Locate platelets.
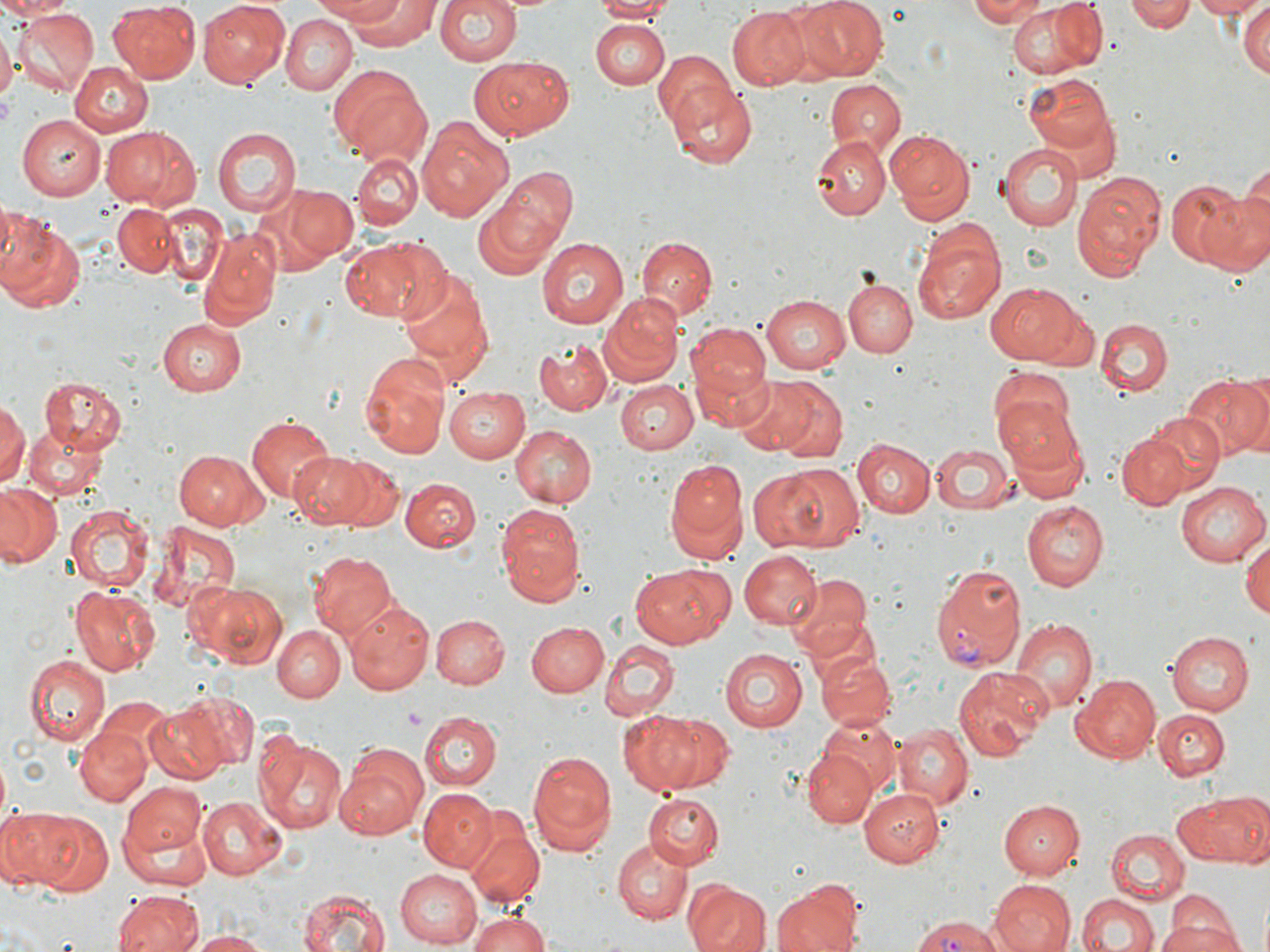
Approximate bounding boxes as named x1/y1/x2/y2 corners in pixels.
Platelets: (x1=0, y1=91, x2=15, y2=131), (x1=402, y1=705, x2=427, y2=728).

Plasmodium vivax-infected red blood cell locations: (x1=930, y1=563, x2=1025, y2=672), (x1=911, y1=915, x2=1009, y2=952). Uninfected red blood cell locations: (x1=0, y1=0, x2=63, y2=19), (x1=197, y1=0, x2=290, y2=87), (x1=304, y1=0, x2=419, y2=26), (x1=325, y1=0, x2=439, y2=49), (x1=434, y1=0, x2=526, y2=67), (x1=591, y1=0, x2=672, y2=21), (x1=796, y1=0, x2=887, y2=80), (x1=969, y1=0, x2=1048, y2=25), (x1=1129, y1=0, x2=1195, y2=32), (x1=1189, y1=0, x2=1267, y2=19), (x1=1005, y1=1, x2=1106, y2=81), (x1=106, y1=3, x2=201, y2=83), (x1=1238, y1=3, x2=1270, y2=81), (x1=728, y1=6, x2=810, y2=89), (x1=15, y1=9, x2=98, y2=96), (x1=281, y1=14, x2=358, y2=95), (x1=590, y1=19, x2=669, y2=91), (x1=0, y1=29, x2=14, y2=103), (x1=652, y1=52, x2=736, y2=134), (x1=470, y1=54, x2=574, y2=139), (x1=69, y1=62, x2=152, y2=137), (x1=329, y1=69, x2=430, y2=163), (x1=1024, y1=73, x2=1119, y2=157), (x1=824, y1=80, x2=906, y2=159), (x1=669, y1=83, x2=757, y2=170), (x1=16, y1=115, x2=105, y2=199), (x1=418, y1=115, x2=515, y2=220), (x1=102, y1=124, x2=197, y2=209), (x1=213, y1=127, x2=300, y2=216), (x1=886, y1=129, x2=976, y2=222), (x1=810, y1=135, x2=890, y2=221), (x1=996, y1=142, x2=1081, y2=232), (x1=351, y1=154, x2=421, y2=230), (x1=490, y1=168, x2=577, y2=261), (x1=1071, y1=172, x2=1165, y2=279), (x1=1165, y1=179, x2=1247, y2=269), (x1=271, y1=182, x2=356, y2=266), (x1=1206, y1=187, x2=1269, y2=276), (x1=472, y1=201, x2=561, y2=282), (x1=157, y1=202, x2=230, y2=286), (x1=113, y1=205, x2=180, y2=278), (x1=0, y1=210, x2=86, y2=314), (x1=198, y1=228, x2=280, y2=332), (x1=912, y1=230, x2=1005, y2=324), (x1=340, y1=237, x2=432, y2=322), (x1=636, y1=237, x2=715, y2=322), (x1=537, y1=239, x2=628, y2=330), (x1=395, y1=264, x2=495, y2=386), (x1=842, y1=279, x2=917, y2=358), (x1=989, y1=282, x2=1085, y2=365), (x1=599, y1=294, x2=684, y2=384), (x1=760, y1=294, x2=851, y2=374), (x1=1040, y1=305, x2=1100, y2=371), (x1=158, y1=317, x2=246, y2=396), (x1=1095, y1=317, x2=1174, y2=396), (x1=686, y1=320, x2=770, y2=417), (x1=535, y1=338, x2=613, y2=414), (x1=361, y1=352, x2=449, y2=460), (x1=987, y1=365, x2=1078, y2=453), (x1=1182, y1=373, x2=1270, y2=459), (x1=732, y1=374, x2=817, y2=455), (x1=40, y1=375, x2=127, y2=453), (x1=762, y1=377, x2=849, y2=461), (x1=616, y1=380, x2=699, y2=455), (x1=443, y1=387, x2=530, y2=463), (x1=996, y1=397, x2=1085, y2=477), (x1=0, y1=399, x2=26, y2=488), (x1=1143, y1=411, x2=1226, y2=493), (x1=246, y1=414, x2=335, y2=504), (x1=23, y1=423, x2=107, y2=498), (x1=508, y1=423, x2=596, y2=509), (x1=1116, y1=433, x2=1190, y2=511), (x1=852, y1=440, x2=935, y2=518), (x1=931, y1=441, x2=1014, y2=514), (x1=173, y1=449, x2=267, y2=530), (x1=288, y1=452, x2=381, y2=529), (x1=332, y1=459, x2=405, y2=532), (x1=663, y1=460, x2=747, y2=557), (x1=747, y1=465, x2=860, y2=553), (x1=400, y1=478, x2=479, y2=551), (x1=1175, y1=482, x2=1267, y2=567), (x1=0, y1=483, x2=63, y2=568), (x1=1022, y1=500, x2=1109, y2=590), (x1=66, y1=504, x2=154, y2=593), (x1=497, y1=504, x2=586, y2=606), (x1=149, y1=522, x2=240, y2=614), (x1=1244, y1=537, x2=1270, y2=620), (x1=739, y1=550, x2=821, y2=630), (x1=310, y1=551, x2=398, y2=643), (x1=629, y1=564, x2=732, y2=648), (x1=788, y1=573, x2=873, y2=658), (x1=190, y1=579, x2=287, y2=669), (x1=70, y1=587, x2=160, y2=675), (x1=344, y1=598, x2=434, y2=694), (x1=430, y1=614, x2=508, y2=690), (x1=1011, y1=618, x2=1097, y2=711), (x1=525, y1=621, x2=609, y2=697), (x1=272, y1=622, x2=347, y2=701), (x1=1166, y1=631, x2=1253, y2=716), (x1=600, y1=641, x2=678, y2=718), (x1=718, y1=648, x2=806, y2=732), (x1=814, y1=653, x2=897, y2=730), (x1=23, y1=654, x2=109, y2=744), (x1=953, y1=665, x2=1054, y2=760), (x1=1070, y1=674, x2=1160, y2=763), (x1=168, y1=690, x2=258, y2=773), (x1=83, y1=696, x2=177, y2=785), (x1=142, y1=702, x2=233, y2=783), (x1=1153, y1=709, x2=1229, y2=779), (x1=621, y1=711, x2=718, y2=794), (x1=416, y1=712, x2=499, y2=791), (x1=816, y1=718, x2=897, y2=796), (x1=895, y1=722, x2=972, y2=809), (x1=75, y1=725, x2=152, y2=807), (x1=257, y1=732, x2=349, y2=836), (x1=335, y1=743, x2=429, y2=839), (x1=802, y1=748, x2=875, y2=827), (x1=527, y1=749, x2=618, y2=857), (x1=116, y1=778, x2=211, y2=874), (x1=859, y1=786, x2=945, y2=868), (x1=418, y1=788, x2=498, y2=870), (x1=1178, y1=789, x2=1270, y2=868), (x1=645, y1=793, x2=725, y2=869), (x1=197, y1=796, x2=288, y2=879), (x1=998, y1=798, x2=1083, y2=878), (x1=4, y1=806, x2=100, y2=891), (x1=465, y1=817, x2=542, y2=905), (x1=1105, y1=830, x2=1191, y2=904), (x1=613, y1=839, x2=690, y2=925), (x1=393, y1=868, x2=485, y2=946), (x1=682, y1=877, x2=772, y2=952), (x1=771, y1=878, x2=861, y2=952), (x1=987, y1=880, x2=1075, y2=952), (x1=294, y1=887, x2=392, y2=952), (x1=115, y1=891, x2=203, y2=952), (x1=1076, y1=892, x2=1160, y2=952), (x1=1157, y1=907, x2=1243, y2=952), (x1=465, y1=910, x2=551, y2=952), (x1=188, y1=930, x2=275, y2=951). Slide-level diagnosis: Plasmodium vivax. One field of a larger specimen. Optical microscopy. May-Grünwald-Giemsa stain. Thin blood smear. Image is 1270×952 pixels. Captured at 1000x magnification.